Give the position of every Plasmodium parasite visible.
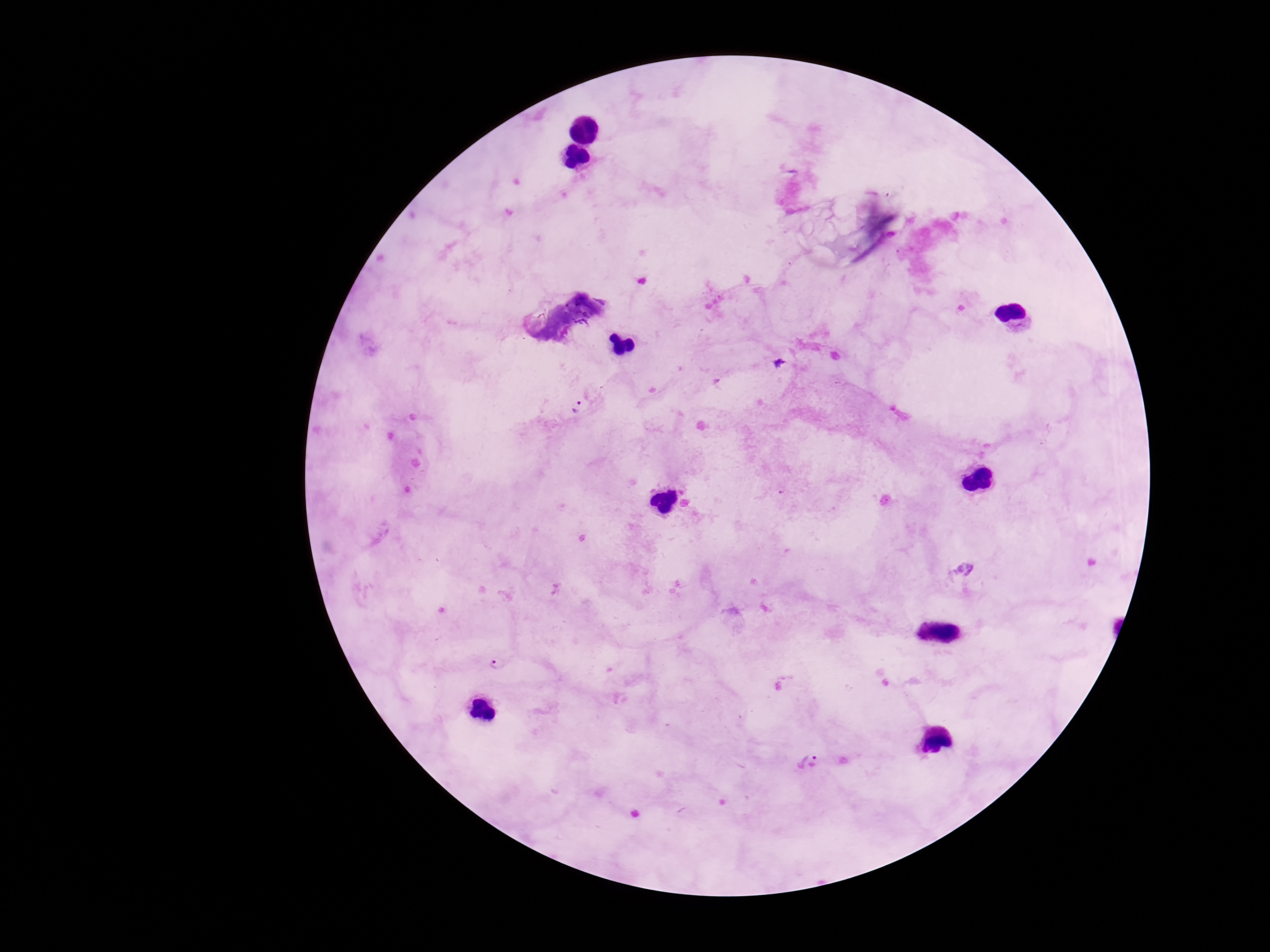

Approximate object centers, in pixels from the top-left corner.
Plasmodium parasites: (x=578, y=405), (x=498, y=663), (x=809, y=761).

Photographed through the microscope eyepiece with a smartphone camera. 100x magnification. Patient malaria status: infected. Image is 1270×952 pixels. Thick peripheral-blood smear. Single field of view. Giemsa stain.